State which parasite is depicted.
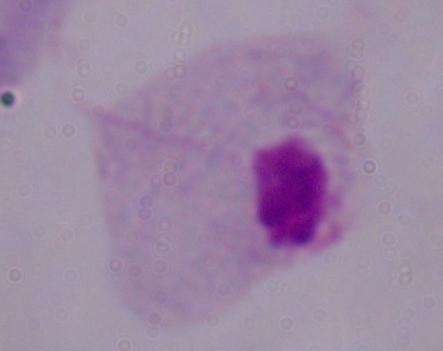

This is a trichomonad.

Micrograph. 1000x magnification.